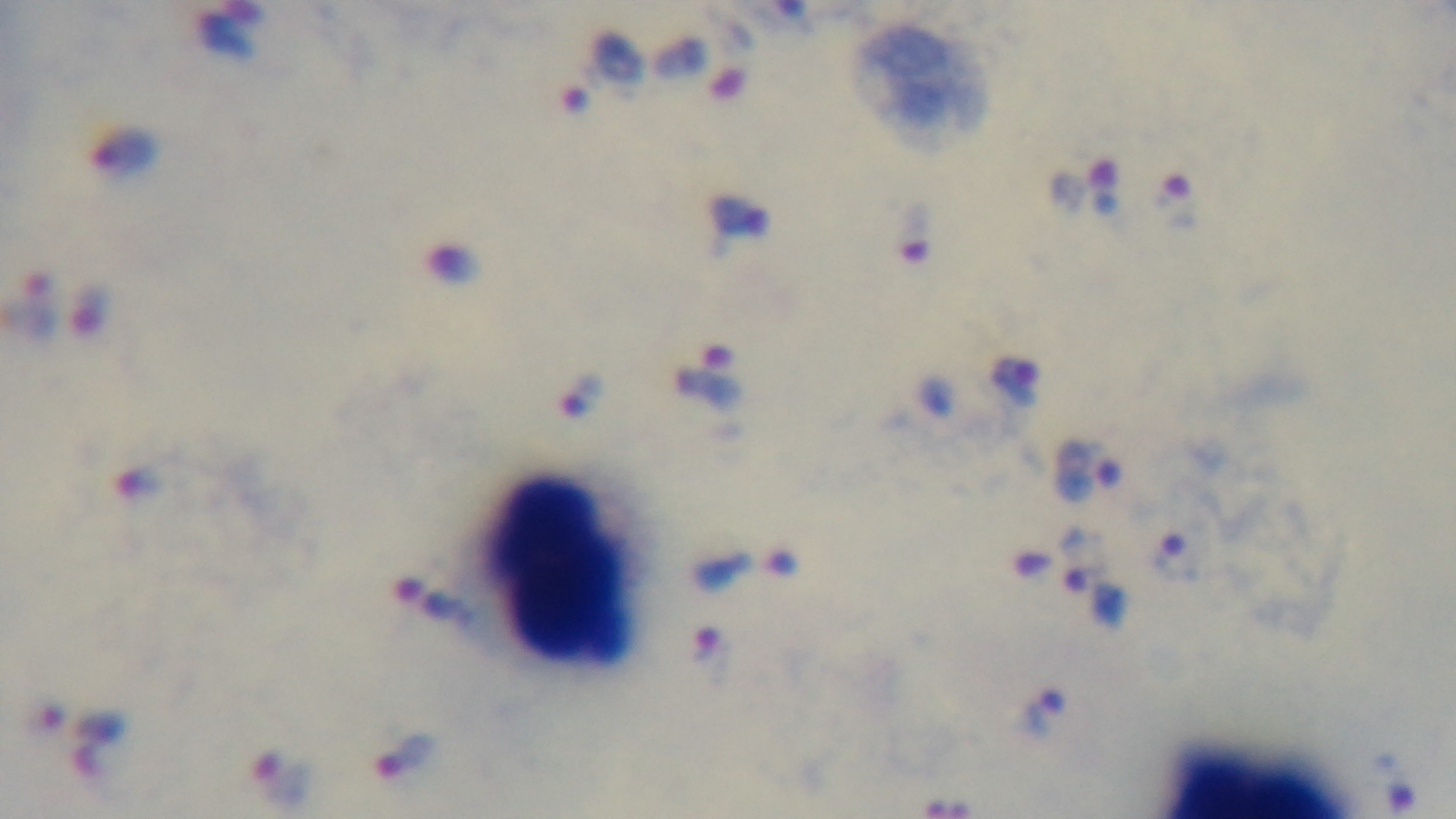
Summary:
  - Preparation: thick blood film
  - Objective: 100x oil immersion
  - Field of view: single
  - Modality: light microscopy
  - Malaria status: infected
  - Stain: Giemsa
  - Capture: mounted 4K digital camera